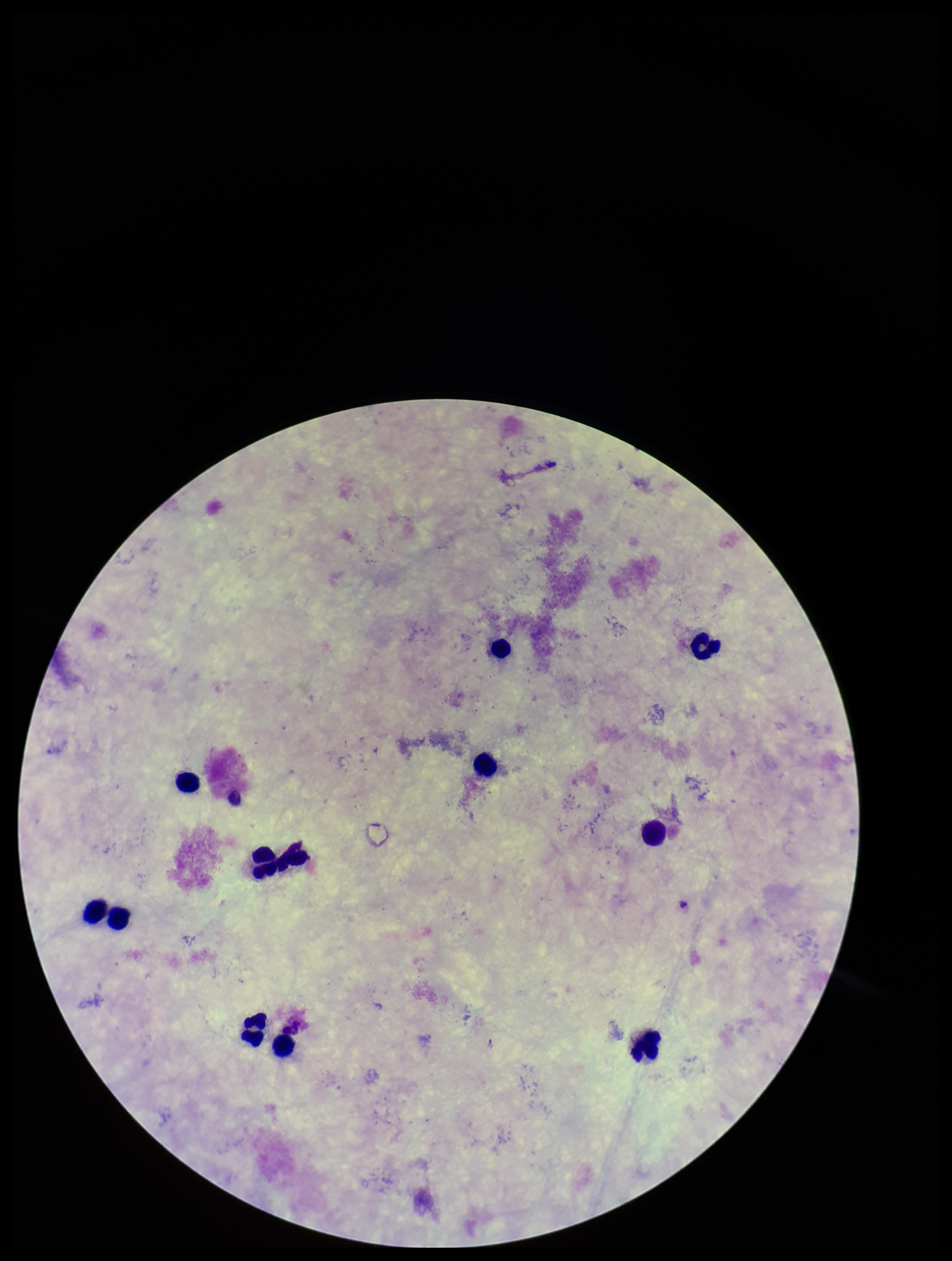 Image is 952×1261 pixels. Preparation: thick blood smear. Parasite count: 0. Plasmodium parasites: none seen. Photographed through the microscope eyepiece with a smartphone camera. Patient malaria status: negative. Single field of view. Leukocyte count: 12. Giemsa stain.